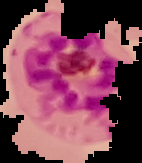
{
  "malaria_status": "parasitized",
  "image_type": "segmented cell region with the area outside set to black",
  "preparation": "thin blood smear",
  "image_size": "142×163 pixels"
}